Locate every leukocyte (white blood cell).
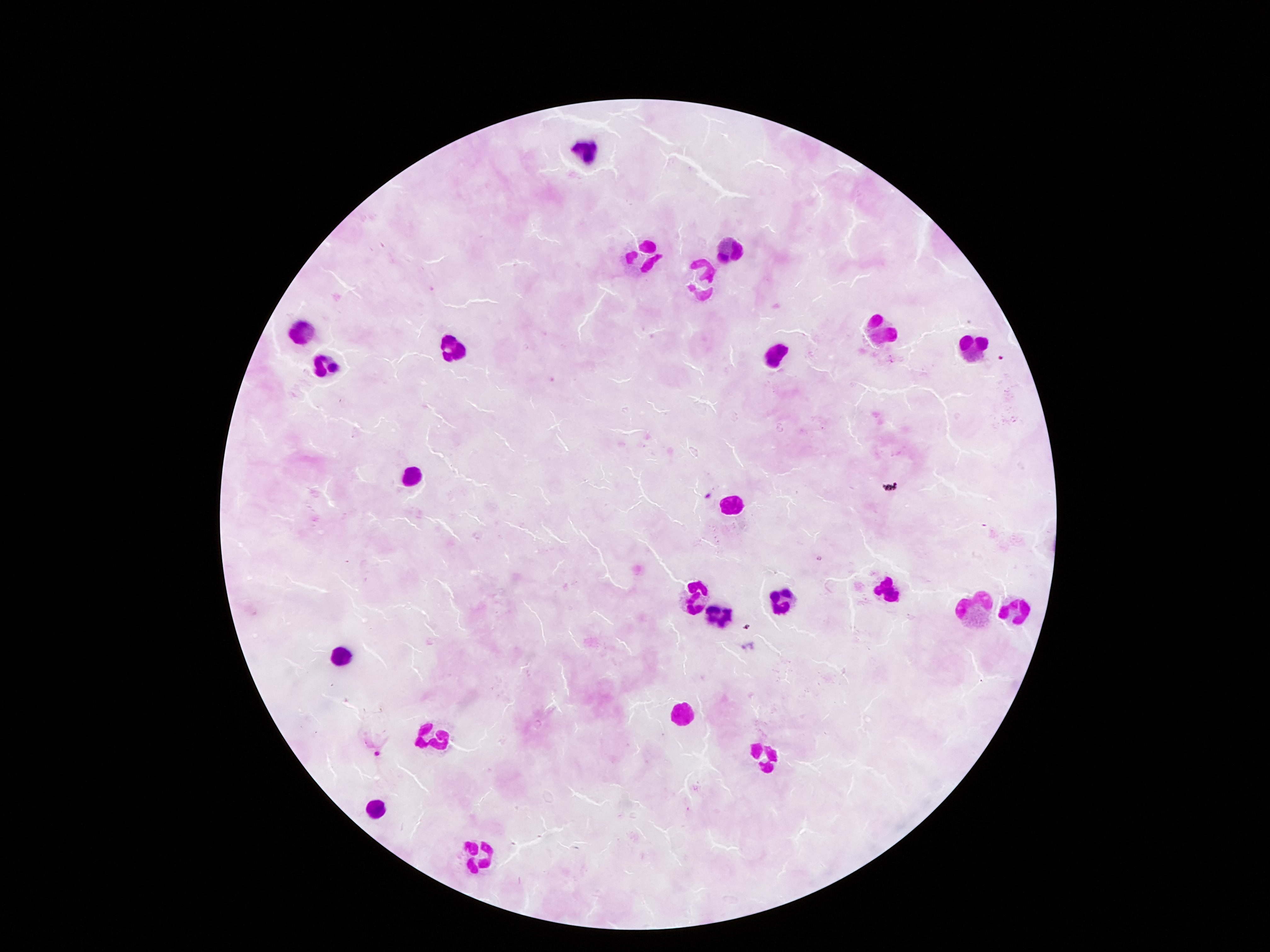
Approximate centers as {x, y} in pixels.
Leukocytes: {734, 245}, {649, 255}, {699, 279}, {879, 327}, {300, 333}, {446, 343}, {974, 347}, {776, 353}, {322, 367}, {410, 474}, {737, 507}, {889, 587}, {689, 588}, {779, 601}, {1019, 609}, {974, 611}, {711, 622}, {337, 652}, {673, 716}, {429, 735}, {765, 757}, {373, 805}, {477, 852}.

Single field of view. 100x magnification. Patient malaria status: not infected. Giemsa stain. Thick blood film. Image is 1270×952 pixels. Smartphone photograph taken through the microscope eyepiece.